Assess this cell for malaria.
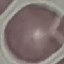
It is uninfected.

stain: Giemsa
preparation: thin blood film
image_type: cell patch, automatically extracted from a larger field of view and resized to 64 × 64 pixels
capture: smartphone through the microscope eyepiece